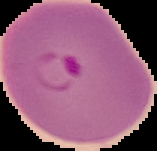
Summary:
  - Image size: 157×151 pixels
  - Result: Plasmodium parasites detected
  - Preparation: thin blood smear
  - Image type: segmented cell region on a black background